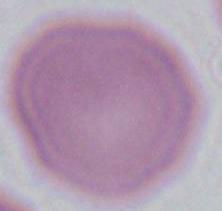
Captured at 1000x magnification. Micrograph. A red blood cell is shown.